Outline each blood parasite and name the species.
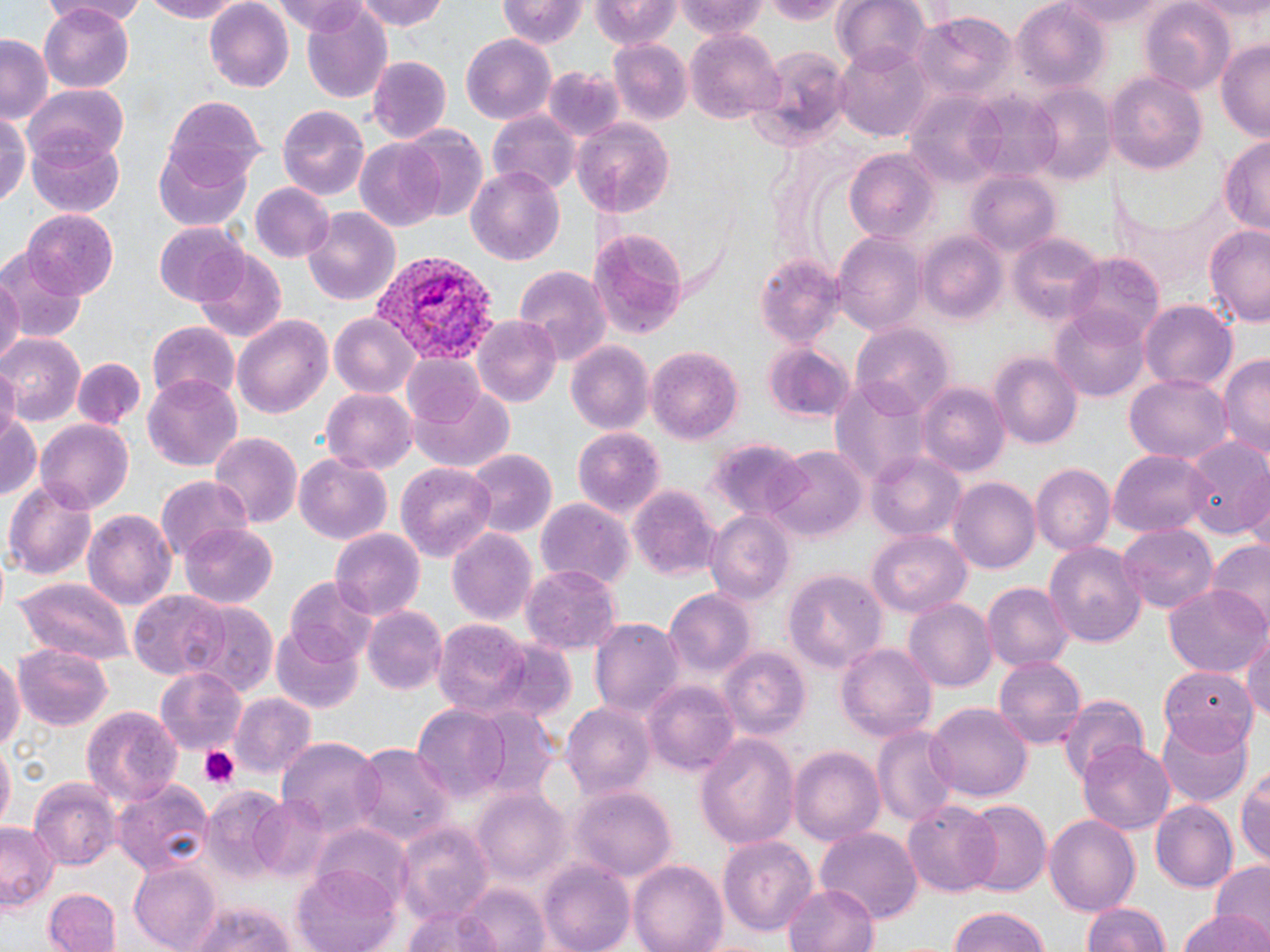

Approximate bounding boxes as [x1, y1, x2, y2] in pixels.
Plasmodium vivax-infected red blood cells: [371, 255, 498, 364].
No Plasmodium falciparum, Plasmodium ovale, Plasmodium malariae, Babesia divergens, or Trypanosoma brucei observed.

Summary:
  - Uninfected red blood cell locations: [59, 0, 150, 24], [135, 0, 252, 23], [271, 0, 374, 35], [356, 0, 451, 33], [588, 0, 681, 49], [679, 0, 770, 41], [757, 0, 847, 23], [832, 0, 931, 72], [1010, 0, 1106, 88], [1055, 0, 1173, 30], [1140, 0, 1233, 93], [494, 1, 587, 48], [40, 2, 135, 89], [204, 2, 294, 92], [299, 7, 392, 105], [911, 13, 1015, 104], [687, 30, 786, 125], [460, 35, 555, 123], [0, 36, 53, 120], [609, 39, 690, 124], [1216, 39, 1270, 144], [834, 41, 931, 143], [746, 47, 852, 151], [367, 56, 451, 143], [544, 64, 623, 143], [1110, 71, 1206, 175], [27, 83, 128, 165], [1024, 84, 1113, 185], [962, 89, 1066, 183], [906, 91, 1015, 188], [163, 96, 266, 184], [279, 105, 369, 198], [487, 110, 578, 195], [0, 112, 29, 210], [573, 117, 676, 216], [401, 123, 488, 220], [28, 133, 124, 216], [356, 138, 448, 234], [1219, 140, 1270, 232], [153, 149, 253, 233], [846, 151, 939, 244], [466, 163, 565, 269], [965, 173, 1061, 258], [250, 182, 335, 264], [303, 206, 401, 306], [22, 209, 118, 297], [1203, 223, 1270, 326], [153, 224, 251, 305], [587, 224, 689, 339], [919, 230, 1005, 323], [834, 233, 926, 335], [1009, 233, 1107, 327], [0, 249, 85, 346], [195, 250, 287, 343], [1067, 252, 1163, 342], [755, 256, 841, 347], [515, 265, 612, 364], [0, 274, 22, 369], [1141, 300, 1235, 391], [1053, 307, 1151, 402], [328, 313, 419, 398], [232, 315, 335, 419], [472, 317, 560, 407], [147, 321, 241, 403], [852, 323, 954, 415], [1, 333, 83, 422], [566, 342, 654, 436], [762, 344, 852, 424], [645, 345, 745, 443], [1219, 353, 1270, 460], [989, 354, 1082, 448], [74, 355, 145, 431], [399, 355, 488, 427], [0, 368, 19, 439], [1125, 371, 1233, 464], [145, 374, 242, 472], [829, 375, 929, 488], [916, 381, 1008, 476], [406, 385, 515, 473], [320, 389, 417, 474], [0, 407, 40, 505], [36, 419, 134, 512], [573, 428, 664, 519], [209, 432, 301, 532], [1180, 434, 1270, 538], [700, 437, 808, 517], [768, 448, 865, 540], [466, 449, 557, 535], [866, 449, 964, 542], [1109, 450, 1212, 536], [294, 454, 393, 544], [396, 462, 498, 563], [1031, 463, 1115, 554], [948, 476, 1039, 574], [155, 477, 253, 563], [7, 480, 97, 577], [629, 483, 720, 581], [534, 498, 633, 589], [82, 508, 175, 610], [706, 511, 795, 605], [180, 523, 278, 607], [1117, 525, 1218, 616], [448, 527, 537, 628], [328, 528, 425, 622], [866, 530, 971, 618], [1206, 539, 1270, 628], [1044, 540, 1149, 648], [525, 563, 622, 656], [784, 571, 888, 677], [284, 576, 383, 663], [13, 577, 134, 666], [981, 582, 1073, 674], [1163, 582, 1269, 679], [129, 589, 229, 679], [664, 589, 754, 677], [904, 599, 997, 692], [181, 603, 277, 696], [362, 605, 449, 695], [590, 617, 684, 719], [432, 619, 539, 721], [270, 624, 363, 714], [1242, 627, 1270, 730], [835, 642, 938, 742], [14, 643, 112, 730], [719, 648, 811, 741], [0, 652, 23, 762], [993, 654, 1087, 751], [1165, 662, 1262, 749], [153, 667, 247, 756], [643, 679, 739, 776], [232, 691, 316, 778], [1057, 691, 1152, 783], [561, 702, 654, 801], [924, 702, 1031, 801], [83, 705, 183, 807], [469, 706, 561, 800], [412, 707, 510, 802], [1155, 716, 1251, 804], [872, 724, 961, 830], [695, 732, 799, 850], [278, 740, 382, 833], [1078, 740, 1177, 833], [350, 743, 453, 843], [788, 745, 885, 846], [0, 747, 12, 831], [1237, 763, 1270, 873], [111, 778, 213, 877], [28, 779, 117, 871], [572, 787, 676, 884], [201, 788, 291, 883], [471, 791, 569, 885], [251, 793, 335, 882], [903, 801, 1003, 895], [961, 801, 1051, 899], [1151, 801, 1235, 890], [1044, 812, 1141, 919], [392, 818, 492, 923], [1, 824, 57, 910], [311, 826, 412, 909], [814, 827, 922, 926], [720, 835, 818, 938], [629, 860, 728, 952], [1210, 860, 1270, 940], [540, 861, 636, 952], [127, 863, 221, 949], [294, 865, 404, 952], [451, 881, 552, 952], [783, 881, 880, 952], [43, 887, 120, 952], [1083, 901, 1172, 952], [185, 902, 300, 952], [398, 902, 517, 952], [943, 907, 1053, 952], [1177, 911, 1267, 952]
  - Platelet locations: [195, 745, 242, 789]
  - Slide-level diagnosis: Plasmodium vivax
  - Field of view: single
  - Preparation: thin blood film
  - Magnification: 1000x
  - Image size: 1270×952 pixels
  - Modality: optical microscopy
  - Stain: May-Grünwald-Giemsa